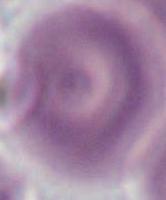

Micrograph. 1000x magnification. A red blood cell is shown.